Locate and identify every blood parasite.
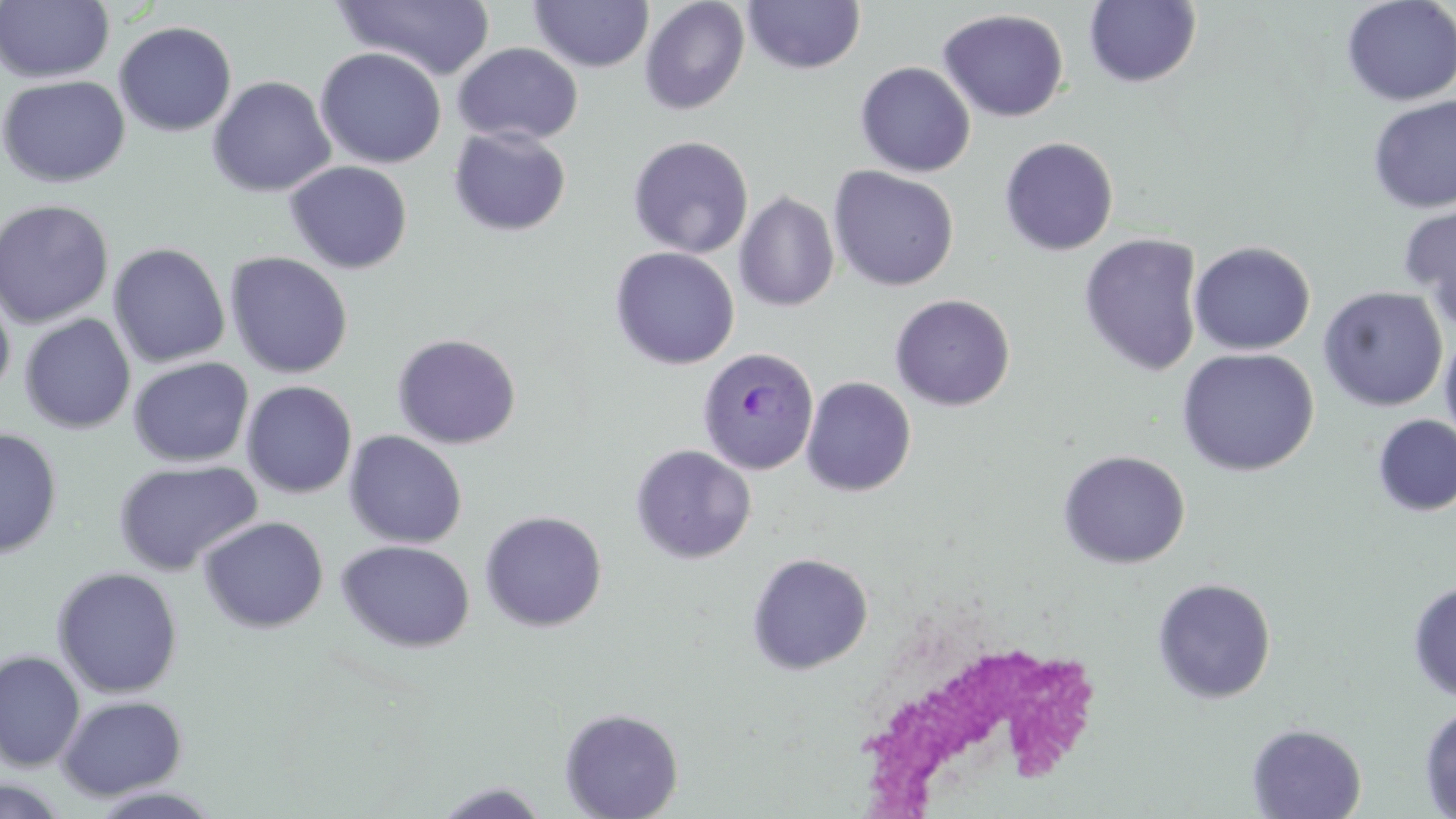
Approximate bounding boxes as [x1, y1, x2, y2] in pixels.
Plasmodium ovale-infected red blood cells: [697, 347, 819, 474].
No Plasmodium falciparum, Plasmodium malariae, Plasmodium vivax, Babesia divergens, or Trypanosoma brucei observed.

slide-level diagnosis = Plasmodium ovale
preparation = thin blood film
stain = May-Grünwald-Giemsa
modality = light microscopy
white blood cell locations = approximate bounding boxes as [x1, y1, x2, y2] in pixels: [861, 645, 1102, 819]
image size = 1456×819 pixels
field of view = one of a larger specimen
magnification = 1000x
uninfected red blood cell locations = approximate bounding boxes as [x1, y1, x2, y2] in pixels: [528, 0, 654, 74], [639, 0, 750, 115], [1341, 0, 1456, 106], [0, 1, 115, 84], [333, 1, 496, 81], [743, 1, 865, 74], [1084, 1, 1202, 88], [938, 8, 1069, 122], [114, 21, 238, 137], [452, 42, 583, 146], [314, 46, 447, 169], [855, 61, 975, 177], [0, 74, 131, 189], [207, 76, 336, 198], [1367, 95, 1456, 214], [448, 125, 572, 237], [627, 135, 754, 259], [999, 136, 1119, 256], [284, 160, 413, 274], [828, 166, 959, 292], [734, 191, 839, 312], [0, 199, 114, 328], [1398, 203, 1456, 330], [1078, 233, 1204, 376], [1188, 241, 1316, 356], [108, 242, 231, 368], [609, 246, 740, 371], [224, 251, 354, 379], [0, 283, 16, 403], [1319, 286, 1448, 412], [889, 294, 1015, 411], [19, 314, 136, 434], [1439, 330, 1456, 450], [392, 333, 521, 450], [1176, 348, 1319, 476], [127, 356, 254, 467], [130, 374, 356, 484], [801, 376, 917, 497], [241, 380, 358, 499], [1373, 414, 1456, 517], [0, 428, 63, 560], [344, 430, 467, 549], [629, 444, 756, 564], [1057, 449, 1191, 569], [112, 459, 263, 577], [479, 510, 608, 632], [198, 516, 328, 634], [336, 539, 475, 652], [746, 552, 874, 675], [51, 566, 183, 698], [1151, 577, 1277, 705], [1407, 582, 1456, 702], [0, 650, 86, 772], [55, 694, 188, 801], [1419, 703, 1456, 819], [559, 707, 684, 819], [1246, 723, 1367, 818], [0, 776, 71, 819], [431, 781, 552, 819], [85, 785, 226, 817]